State the blood parasite species.
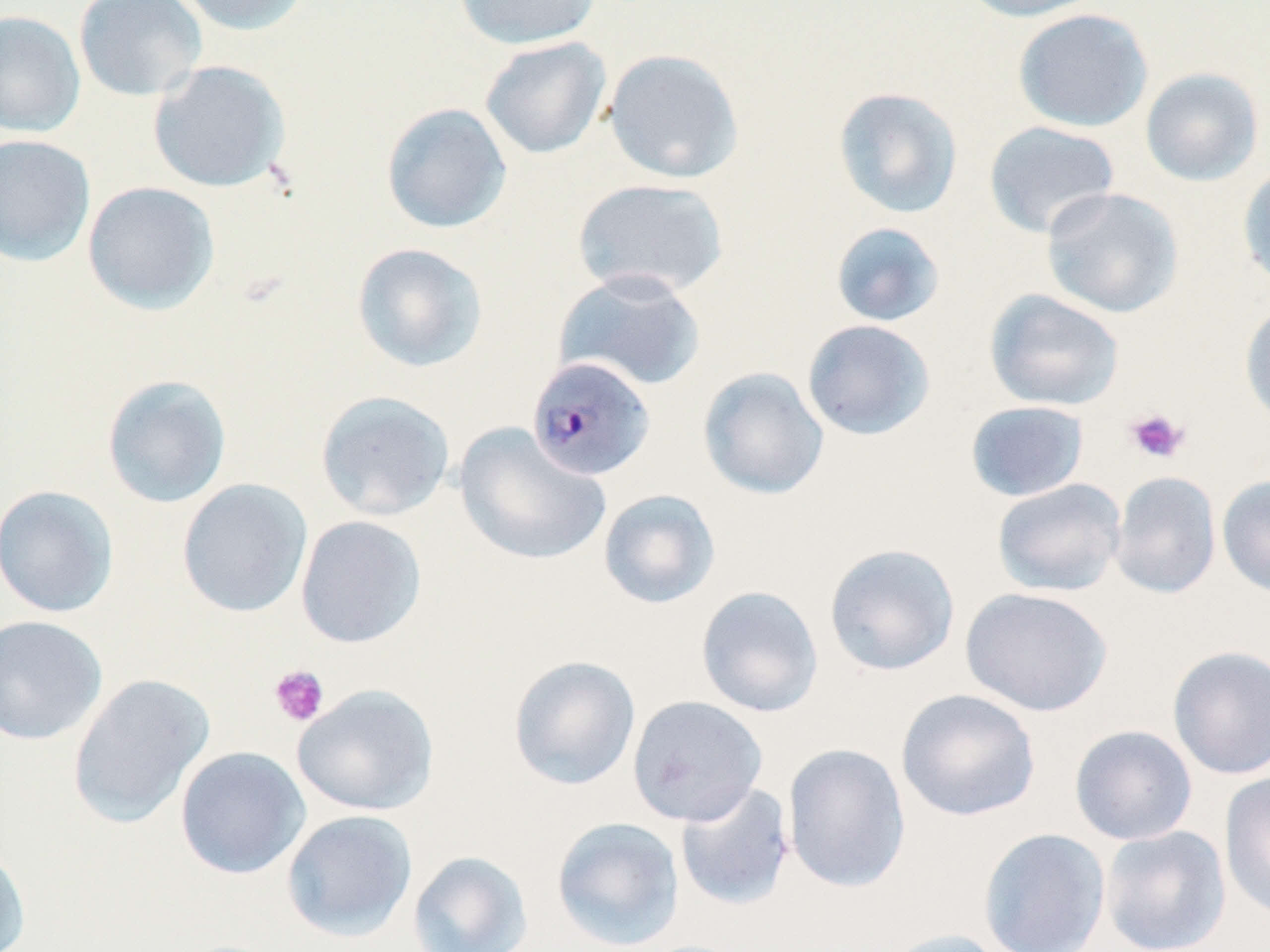

Plasmodium malariae.

stain = May-Grünwald-Giemsa
platelet locations = approximate bounding boxes as (x1,y1)-(x2,y2) corner pairs in pixels: (1124,408)-(1190,464), (269,664)-(329,727)
magnification = 1000x
Plasmodium malariae-infected red blood cell locations = approximate bounding boxes as (x1,y1)-(x2,y2) corner pairs in pixels: (526,355)-(657,482)
preparation = thin blood smear
uninfected red blood cell locations = approximate bounding boxes as (x1,y1)-(x2,y2) corner pairs in pixels: (73,0)-(208,102), (171,0)-(313,36), (454,0)-(601,50), (956,0)-(1103,22), (1013,8)-(1153,132), (0,10)-(85,137), (479,36)-(612,159), (603,48)-(744,184), (147,60)-(291,194), (1139,67)-(1264,187), (832,86)-(964,219), (381,102)-(513,234), (983,120)-(1120,240), (0,134)-(96,267), (1237,163)-(1270,292), (572,177)-(730,300), (82,181)-(220,314), (1040,187)-(1184,318), (830,221)-(946,327), (351,242)-(488,373), (553,269)-(707,392), (984,289)-(1125,412), (1239,302)-(1270,427), (802,319)-(936,441), (697,367)-(830,500), (101,374)-(232,509), (315,390)-(455,521), (965,400)-(1090,502), (454,423)-(610,567), (1109,470)-(1222,599), (1217,475)-(1270,598), (991,478)-(1127,597), (177,479)-(313,618), (0,484)-(119,618), (598,488)-(721,609), (295,515)-(427,649), (824,543)-(961,677), (695,585)-(825,718), (960,586)-(1114,717), (0,615)-(108,745), (1167,644)-(1270,780), (507,655)-(641,791), (67,674)-(214,828), (292,683)-(439,816), (895,688)-(1041,822), (627,695)-(768,826), (1069,724)-(1198,845), (782,742)-(912,894), (175,746)-(311,879), (1219,770)-(1270,924), (674,782)-(796,911), (281,809)-(418,942), (551,815)-(685,951), (1098,825)-(1231,952), (977,828)-(1111,952), (0,840)-(32,952), (407,850)-(534,952), (874,928)-(1015,952)
field of view = single
image size = 1270×952 pixels
modality = optical microscopy